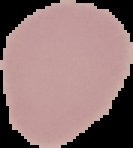

Summary:
  - Image size: 133×148 pixels
  - Preparation: thin blood film
  - Image type: segmented cell region on a black background
  - Result: no Plasmodium parasites seen